Describe the morphology of the erythrocytes.
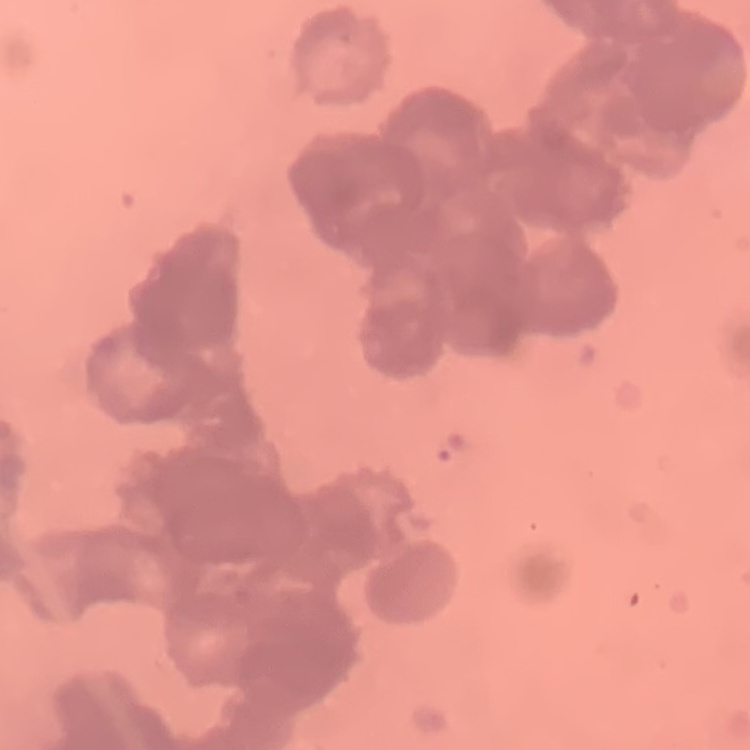
Rouleaux formation.

Thin blood smear. One tile cut from a larger photomicrograph. Field's or Giemsa stain.